Classify this cell by malaria status.
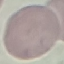
It is uninfected.

{
  "stain": "Giemsa",
  "capture": "smartphone through the microscope eyepiece",
  "preparation": "thin blood smear",
  "image_type": "automatically extracted cell patch, resized to 64 × 64 pixels"
}